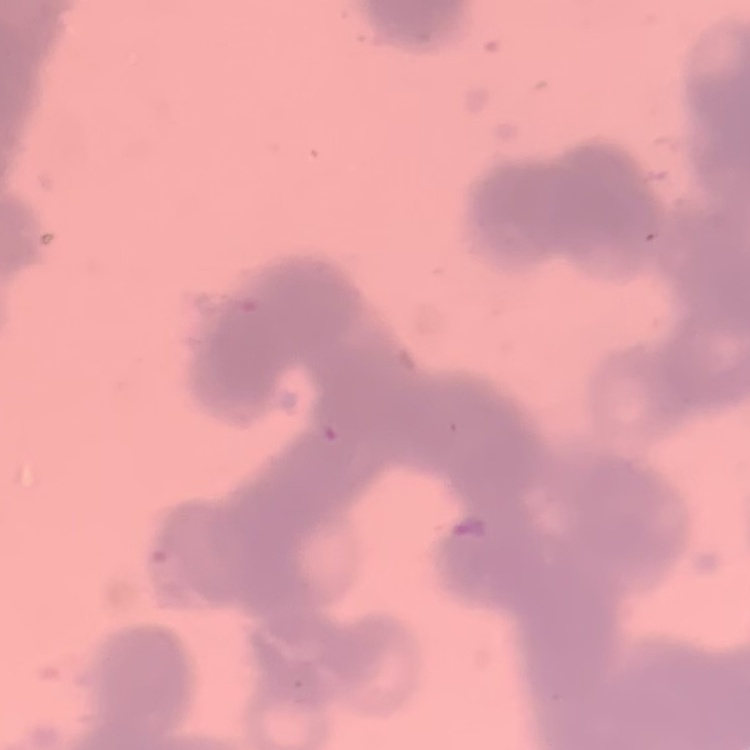
The red blood cells show rouleaux formation. One tile cut from a larger photomicrograph. Stained with either Field's or Giemsa. Thin peripheral smear.